Locate every Plasmodium parasite.
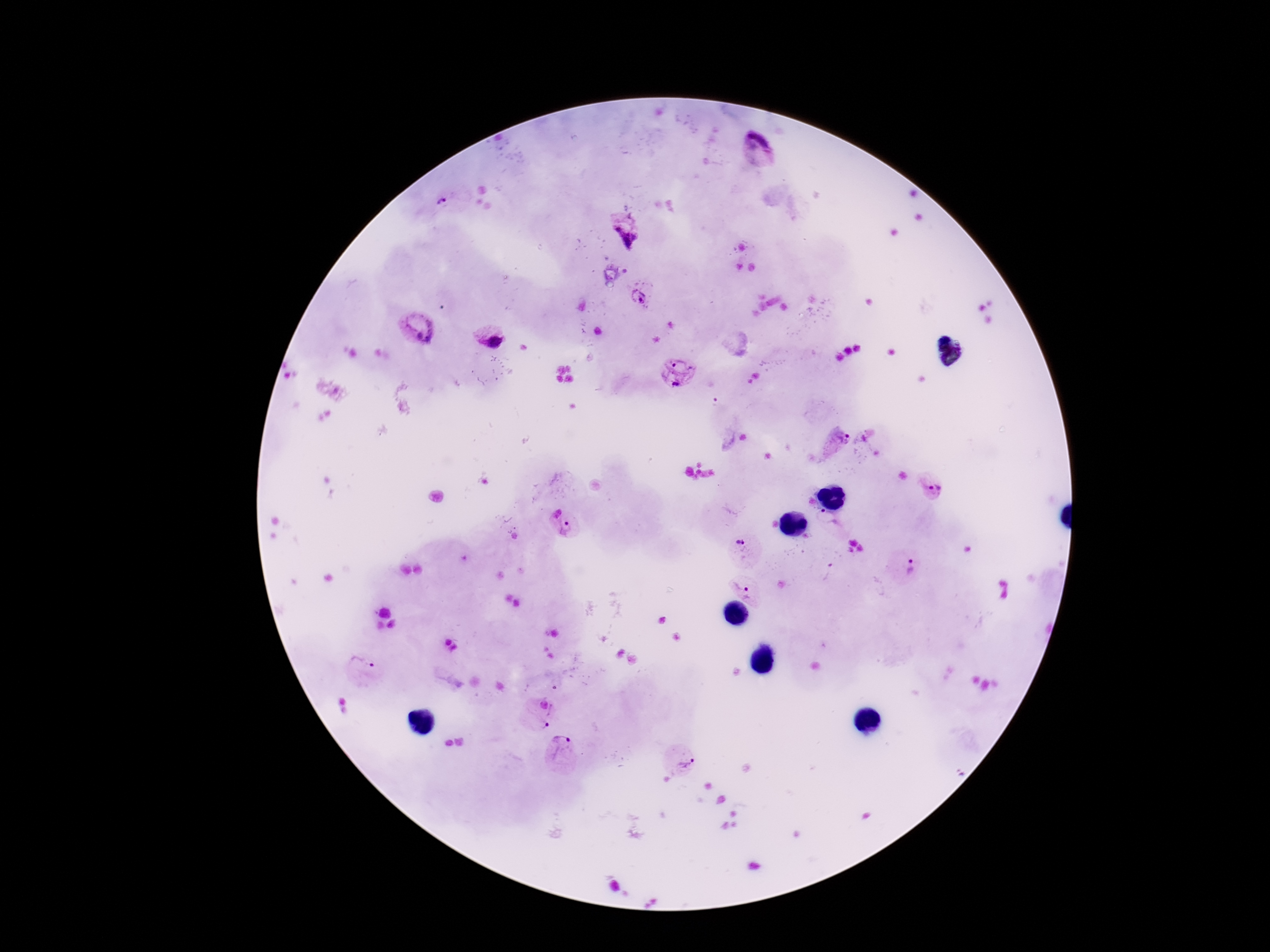
Approximate centers as (x, y) in pixels.
Plasmodium parasites: (758, 150), (443, 200), (627, 236), (639, 297), (416, 329), (489, 336), (678, 371), (837, 442), (935, 487), (556, 513), (828, 521), (567, 530), (739, 542), (909, 568), (746, 593), (362, 666), (543, 705), (542, 726), (562, 742), (689, 763).

patient malaria status = positive
image size = 1270×952 pixels
preparation = thick peripheral-blood smear
magnification = 100x
field of view = one from this slide
stain = Giemsa
capture = smartphone camera through the microscope eyepiece